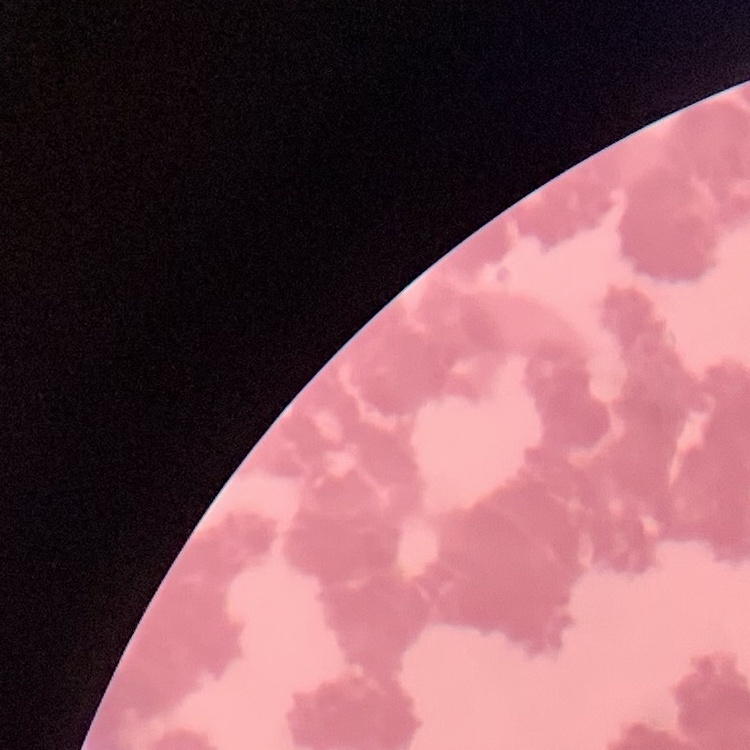

Summary:
  - Red blood cell morphology: rouleaux formation
  - Stain: Field's or Giemsa
  - Preparation: thin peripheral smear
  - Image type: one tile cut from a larger photomicrograph